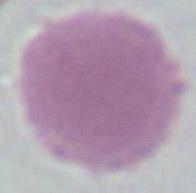

{
  "magnification": "1000x",
  "modality": "micrograph",
  "identification": "erythrocyte"
}